Comment on the morphology of the red blood cells.
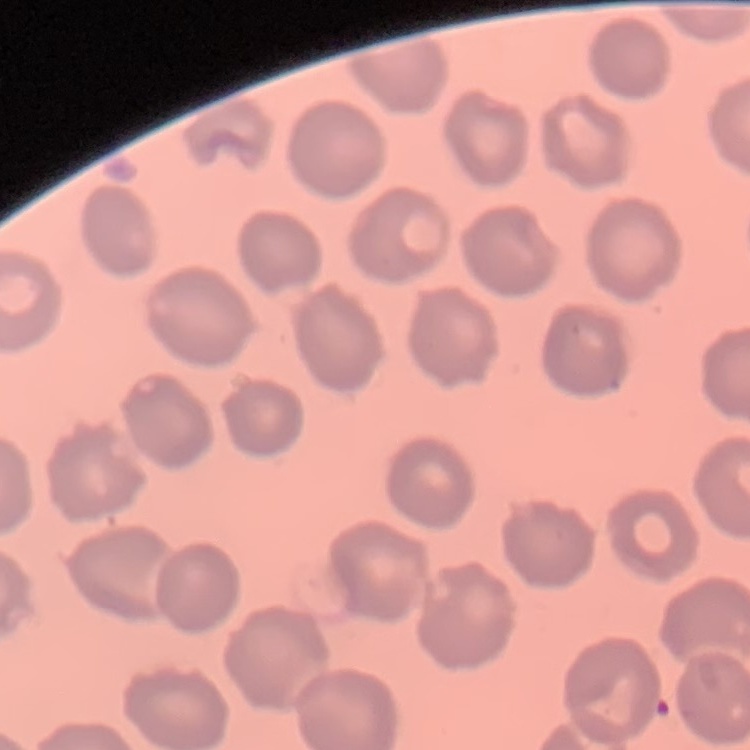

They show no rouleaux formation.

image type = square crop of a larger photomicrograph
preparation = thin blood smear
stain = Field's or Giemsa